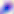

identification = Toxoplasma gondii
magnification = 400x
modality = photomicrograph